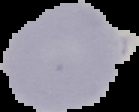 Image is 139×112 pixels. From a thin blood smear. Malaria status: uninfected. Segmented cell region on a black background.